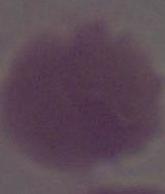

Summary:
  - Identification: erythrocyte
  - Magnification: 1000x
  - Modality: micrograph